Assess the morphology of the erythrocytes.
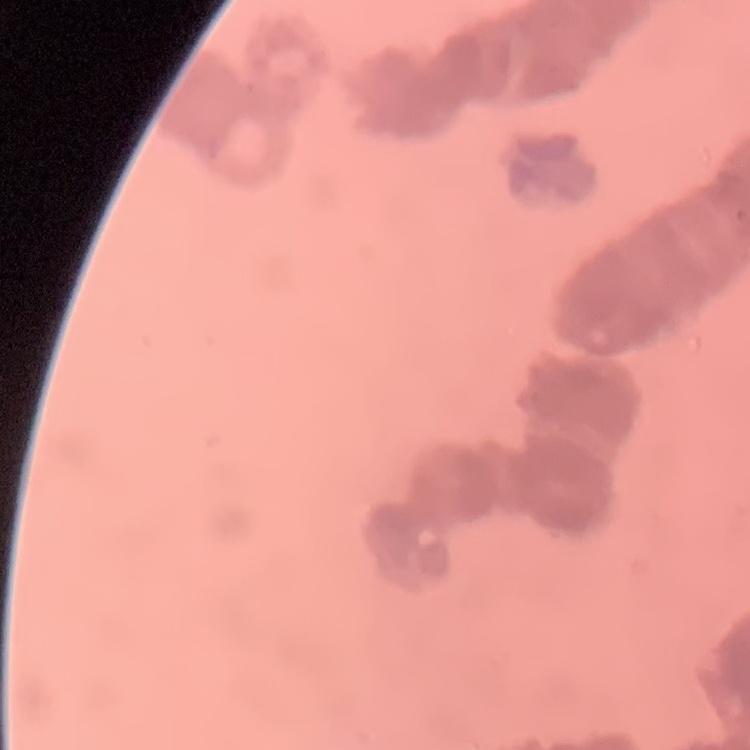
Rouleaux formation.

preparation = thin blood film
image type = one tile cut from a larger photomicrograph
stain = Field's or Giemsa